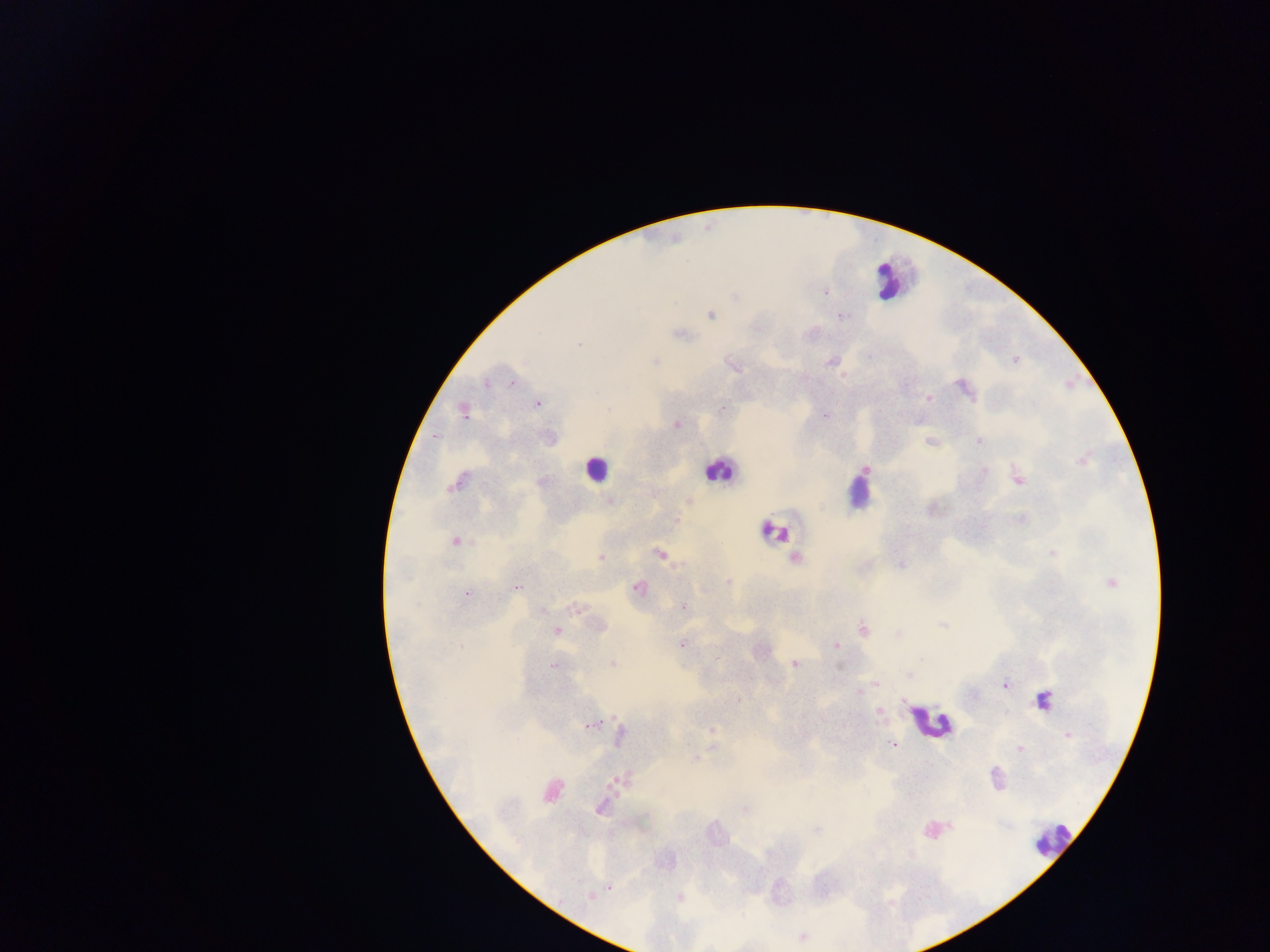
{
  "country": "Ghana",
  "preparation": "thick blood film",
  "leukocyte_locations": "approximate centers as [x, y] in pixels: [885, 280], [595, 468], [717, 470], [857, 494], [773, 531], [929, 722], [1054, 839]",
  "field_of_view": "single",
  "image_size": "1270×952 pixels",
  "capture": "mobile-phone photograph through a microscope",
  "malaria_parasite_locations": "approximate centers as [x, y] in pixels: [824, 292], [734, 297], [711, 315], [842, 316], [679, 334], [580, 344], [1015, 359], [655, 362], [830, 362], [733, 366], [843, 375], [512, 382], [486, 383], [963, 387], [928, 398], [537, 404], [722, 408], [607, 410], [463, 411], [825, 416], [676, 425], [930, 441], [979, 442], [1083, 461], [865, 470], [984, 470], [1018, 479], [457, 483], [609, 500], [688, 501], [931, 508], [456, 541], [660, 554], [1052, 554], [601, 558], [795, 558], [901, 565], [728, 581], [1111, 583], [518, 588], [637, 588], [467, 594], [683, 607], [575, 609], [543, 611], [942, 625], [600, 626], [863, 628], [557, 630], [899, 635], [682, 644], [835, 646], [921, 658], [612, 664], [795, 664], [553, 666], [908, 675], [876, 684], [1005, 684], [858, 693], [738, 699], [1043, 700], [903, 702], [879, 712], [589, 726], [712, 729], [619, 735], [1067, 735], [893, 745], [713, 747], [1019, 748], [694, 759], [616, 781], [551, 792], [601, 808], [745, 809], [815, 830], [610, 887], [589, 897], [679, 898]"
}